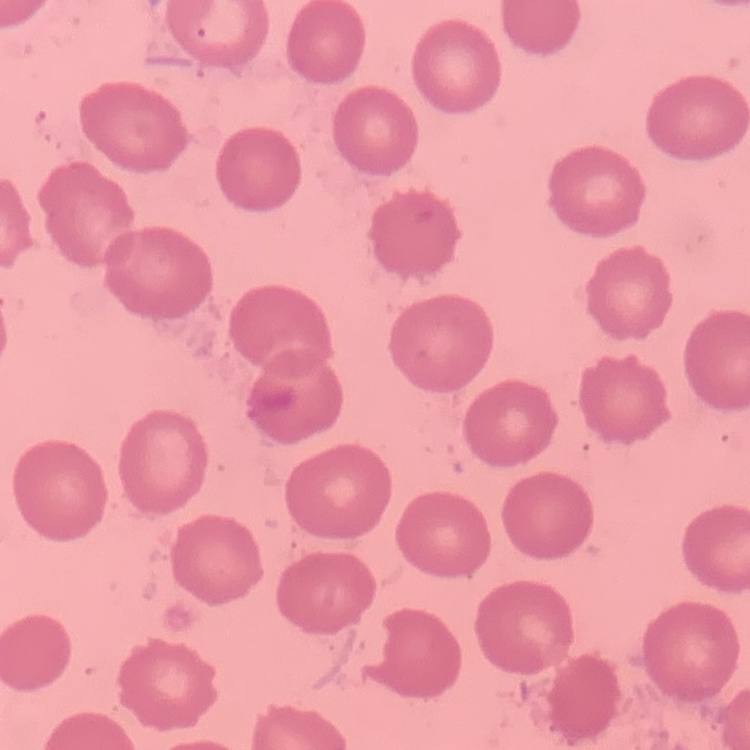

red blood cell morphology = no rouleaux formation
preparation = thin peripheral smear
stain = Field's or Giemsa
image type = one tile cut from a larger photomicrograph